Comment on the morphology of the red blood cells.
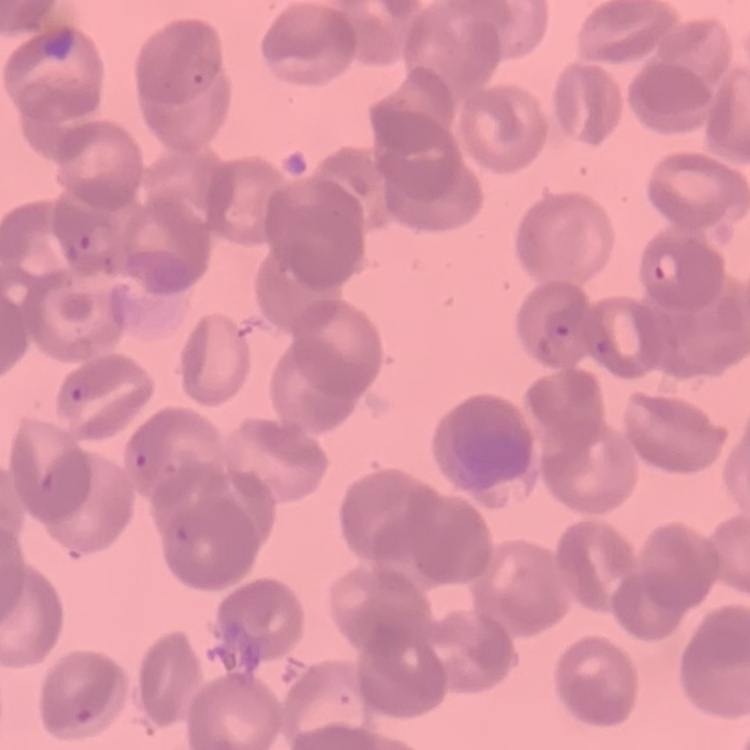

Rouleaux formation.

Summary:
  - Image type: square crop of a larger photomicrograph
  - Preparation: thin peripheral smear
  - Stain: Field's or Giemsa